Classify this cell by malaria status.
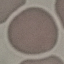
It is uninfected.

Summary:
  - Capture: smartphone through the microscope eyepiece
  - Image type: automatically extracted cell patch, resized to 64 × 64 pixels
  - Preparation: thin smear
  - Stain: Giemsa